Outline each blood parasite and name the species.
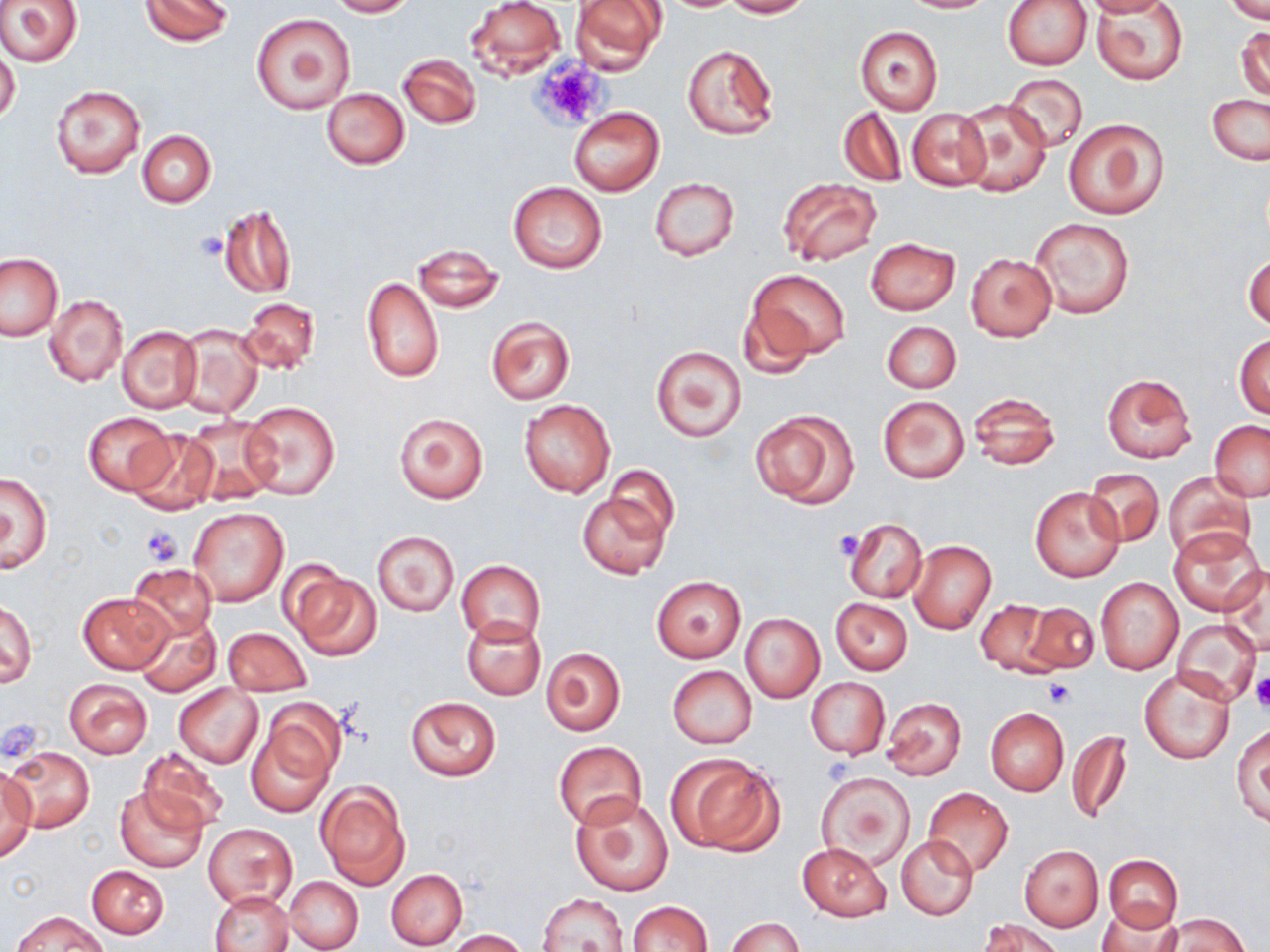

No blood parasites seen.

Approximate bounding boxes as [x1, y1, x2, y2] in pixels. Uninfected red blood cell locations: [0, 0, 83, 68], [140, 0, 233, 46], [326, 0, 417, 17], [465, 0, 566, 80], [570, 0, 667, 74], [720, 0, 812, 18], [898, 0, 995, 13], [1001, 0, 1091, 70], [1084, 0, 1171, 16], [1224, 1, 1270, 24], [1094, 3, 1188, 86], [251, 12, 355, 113], [1236, 25, 1270, 102], [855, 26, 943, 113], [682, 44, 778, 140], [0, 50, 20, 126], [398, 54, 481, 129], [1004, 74, 1087, 153], [49, 84, 146, 180], [321, 87, 410, 168], [1207, 95, 1270, 165], [955, 98, 1052, 197], [568, 107, 663, 197], [837, 107, 907, 187], [907, 109, 991, 191], [1062, 117, 1169, 220], [137, 129, 216, 207], [649, 177, 739, 262], [778, 177, 883, 268], [509, 181, 608, 274], [220, 205, 296, 298], [1029, 217, 1134, 319], [864, 237, 961, 315], [410, 242, 503, 312], [1243, 251, 1270, 330], [0, 252, 64, 342], [966, 253, 1057, 341], [748, 270, 851, 360], [362, 277, 443, 383], [44, 294, 128, 388], [239, 297, 321, 375], [737, 298, 817, 380], [485, 316, 574, 404], [881, 320, 961, 393], [174, 322, 264, 418], [117, 325, 202, 413], [1234, 334, 1270, 418], [651, 345, 747, 442], [1102, 372, 1197, 463], [968, 391, 1061, 471], [877, 395, 970, 483], [519, 398, 615, 498], [242, 399, 341, 500], [750, 408, 857, 508], [84, 412, 176, 494], [394, 412, 489, 503], [182, 415, 279, 506], [1209, 422, 1270, 501], [126, 427, 218, 514], [605, 467, 679, 543], [1084, 469, 1163, 546], [1, 471, 54, 572], [1165, 472, 1256, 565], [1028, 487, 1126, 583], [577, 491, 671, 580], [189, 507, 288, 607], [843, 517, 928, 603], [1168, 527, 1264, 613], [372, 530, 459, 616], [908, 540, 996, 634], [456, 560, 545, 644], [126, 563, 217, 642], [1220, 564, 1270, 655], [284, 566, 381, 661], [652, 577, 745, 662], [1096, 577, 1184, 674], [76, 591, 173, 674], [831, 597, 913, 673], [976, 599, 1058, 675], [1, 600, 36, 688], [1022, 601, 1100, 674], [133, 613, 220, 697], [739, 613, 824, 703], [461, 615, 546, 700], [1171, 620, 1260, 703], [222, 627, 311, 694], [541, 647, 625, 736], [667, 666, 756, 749], [1140, 669, 1235, 765], [804, 677, 889, 759], [64, 678, 153, 758], [173, 684, 263, 768], [405, 696, 501, 780], [880, 696, 968, 782], [247, 706, 341, 817], [986, 707, 1068, 796], [1232, 724, 1269, 825], [1067, 730, 1131, 825], [554, 741, 647, 830], [136, 745, 232, 834], [4, 746, 94, 834], [667, 752, 784, 856], [0, 771, 36, 861], [817, 771, 916, 870], [316, 781, 410, 889], [115, 785, 207, 872], [924, 787, 1013, 877], [571, 795, 674, 897], [203, 823, 297, 909], [897, 835, 978, 920], [798, 843, 891, 921], [1019, 846, 1103, 930], [1104, 854, 1183, 931], [87, 865, 168, 939], [386, 869, 468, 949], [285, 876, 362, 951], [210, 891, 292, 952], [536, 892, 630, 952], [627, 900, 714, 952], [1096, 905, 1183, 952], [13, 912, 107, 952], [1157, 914, 1248, 952], [725, 917, 802, 952], [978, 918, 1063, 952], [446, 930, 530, 951]. Platelet locations: [535, 58, 604, 129], [196, 233, 226, 261], [142, 525, 183, 566], [834, 532, 863, 560], [1252, 677, 1270, 712], [1045, 679, 1075, 707], [823, 756, 860, 785]. Slide-level diagnosis: negative for blood parasites. Thin blood film. Single field of view. Optical microscopy. Image is 1270×952 pixels. Captured at 1000x magnification. May-Grünwald-Giemsa-stained preparation.